Classify this cell by malaria status.
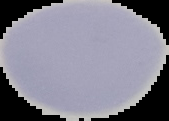

Uninfected.

preparation = thin blood film
image type = cell region segmented out of the field of view; surrounding area masked to black
image size = 169×121 pixels